Name the parasite shown.
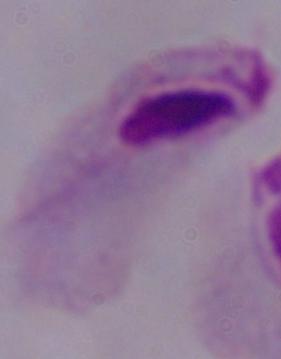

A trichomonad.

Micrograph. 1000x magnification.